Outline each blood parasite and name the species.
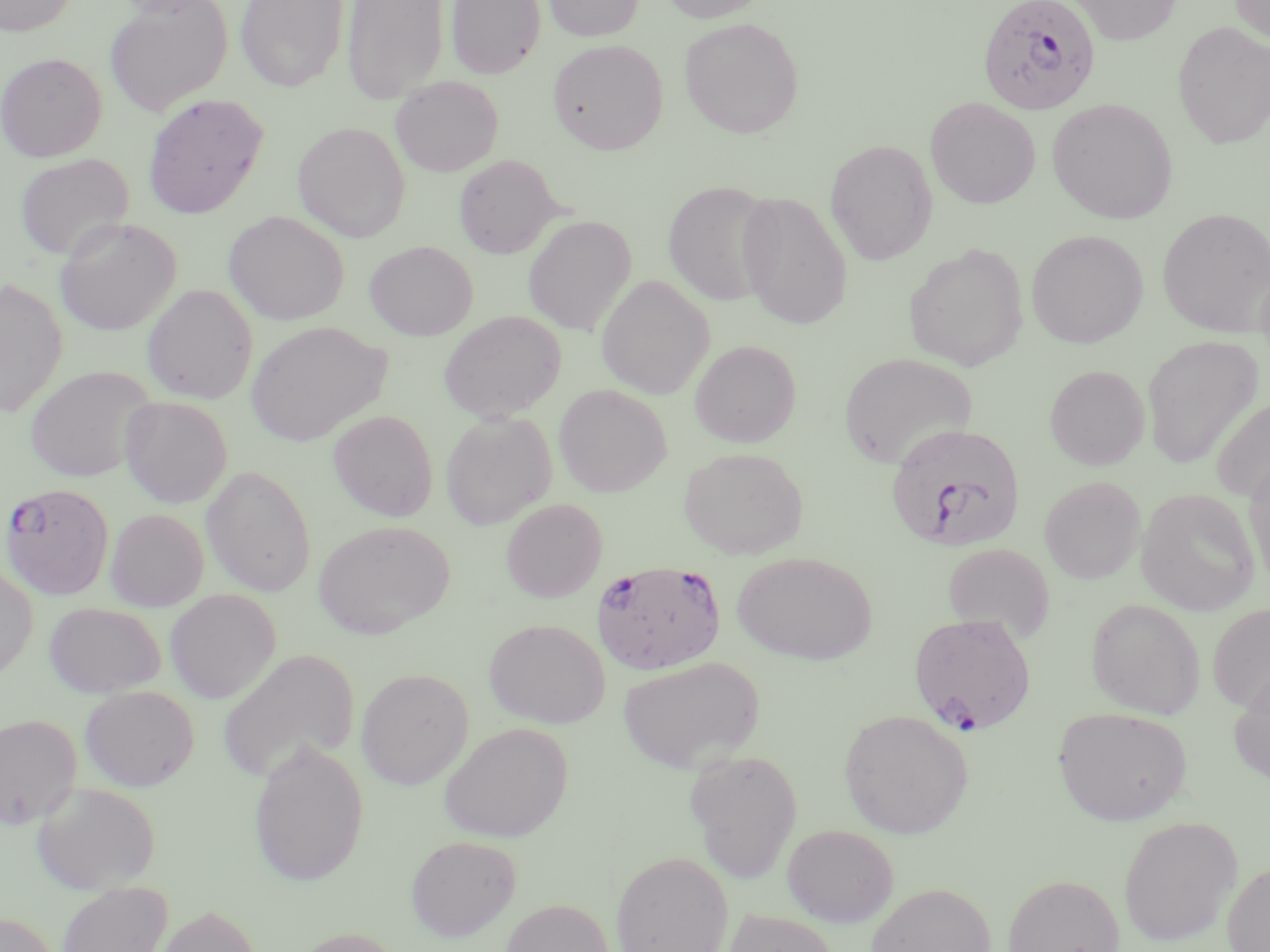
Approximate bounding boxes as named x1/y1/x2/y2 corners in pixels.
Plasmodium falciparum-infected red blood cells: (x1=977, y1=0, x2=1101, y2=115), (x1=885, y1=423, x2=1026, y2=553), (x1=1, y1=482, x2=114, y2=599), (x1=591, y1=559, x2=727, y2=674), (x1=908, y1=612, x2=1036, y2=735).
No Plasmodium ovale, Plasmodium malariae, Plasmodium vivax, Babesia divergens, or Trypanosoma brucei observed.

Uninfected red blood cell locations: (x1=0, y1=0, x2=79, y2=36), (x1=235, y1=0, x2=348, y2=92), (x1=342, y1=0, x2=449, y2=105), (x1=446, y1=0, x2=545, y2=79), (x1=544, y1=0, x2=644, y2=41), (x1=658, y1=0, x2=770, y2=23), (x1=1068, y1=0, x2=1182, y2=45), (x1=1229, y1=0, x2=1270, y2=46), (x1=104, y1=1, x2=232, y2=117), (x1=679, y1=17, x2=804, y2=138), (x1=1172, y1=21, x2=1270, y2=149), (x1=548, y1=39, x2=668, y2=154), (x1=0, y1=52, x2=107, y2=161), (x1=391, y1=76, x2=503, y2=176), (x1=142, y1=94, x2=269, y2=218), (x1=925, y1=97, x2=1041, y2=209), (x1=1047, y1=99, x2=1177, y2=224), (x1=292, y1=121, x2=410, y2=242), (x1=825, y1=139, x2=938, y2=265), (x1=15, y1=153, x2=134, y2=262), (x1=454, y1=155, x2=560, y2=258), (x1=662, y1=179, x2=777, y2=306), (x1=736, y1=191, x2=853, y2=330), (x1=1157, y1=207, x2=1270, y2=337), (x1=224, y1=211, x2=349, y2=325), (x1=523, y1=215, x2=637, y2=336), (x1=54, y1=218, x2=181, y2=337), (x1=1026, y1=229, x2=1148, y2=349), (x1=365, y1=241, x2=478, y2=340), (x1=903, y1=243, x2=1029, y2=372), (x1=596, y1=275, x2=715, y2=399), (x1=0, y1=277, x2=67, y2=419), (x1=142, y1=284, x2=258, y2=404), (x1=438, y1=310, x2=567, y2=422), (x1=246, y1=321, x2=393, y2=446), (x1=1141, y1=334, x2=1263, y2=469), (x1=689, y1=340, x2=801, y2=447), (x1=838, y1=352, x2=978, y2=469), (x1=1044, y1=364, x2=1150, y2=471), (x1=24, y1=365, x2=157, y2=482), (x1=554, y1=384, x2=671, y2=497), (x1=1211, y1=395, x2=1270, y2=504), (x1=119, y1=396, x2=233, y2=508), (x1=327, y1=409, x2=438, y2=521), (x1=440, y1=411, x2=556, y2=530), (x1=678, y1=446, x2=809, y2=559), (x1=1244, y1=456, x2=1270, y2=592), (x1=201, y1=465, x2=316, y2=597), (x1=1040, y1=475, x2=1145, y2=584), (x1=1136, y1=489, x2=1260, y2=615), (x1=500, y1=498, x2=607, y2=602), (x1=105, y1=508, x2=208, y2=611), (x1=313, y1=520, x2=454, y2=638), (x1=942, y1=543, x2=1055, y2=641), (x1=731, y1=550, x2=877, y2=664), (x1=0, y1=565, x2=38, y2=680), (x1=165, y1=589, x2=281, y2=703), (x1=1086, y1=598, x2=1205, y2=719), (x1=44, y1=601, x2=165, y2=698), (x1=1208, y1=604, x2=1270, y2=715), (x1=484, y1=619, x2=610, y2=729), (x1=217, y1=647, x2=359, y2=783), (x1=617, y1=655, x2=765, y2=773), (x1=357, y1=668, x2=473, y2=789), (x1=1229, y1=671, x2=1270, y2=789), (x1=80, y1=686, x2=199, y2=790), (x1=1053, y1=706, x2=1192, y2=825), (x1=839, y1=709, x2=973, y2=838), (x1=0, y1=713, x2=82, y2=828), (x1=440, y1=722, x2=572, y2=843), (x1=248, y1=739, x2=369, y2=887), (x1=684, y1=748, x2=803, y2=883), (x1=31, y1=781, x2=162, y2=893), (x1=1117, y1=816, x2=1242, y2=947), (x1=782, y1=824, x2=898, y2=927), (x1=406, y1=834, x2=521, y2=941), (x1=609, y1=850, x2=733, y2=952), (x1=1222, y1=859, x2=1270, y2=952), (x1=1003, y1=873, x2=1125, y2=952), (x1=56, y1=881, x2=173, y2=952), (x1=866, y1=883, x2=996, y2=952), (x1=500, y1=899, x2=614, y2=952), (x1=157, y1=904, x2=262, y2=952), (x1=721, y1=908, x2=841, y2=952), (x1=0, y1=912, x2=60, y2=952). Slide-level diagnosis: Plasmodium falciparum. Image is 1270×952 pixels. Thin blood film. Single field of view. May-Grünwald-Giemsa stain. Captured at 1000x magnification. Optical microscopy.